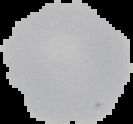 Image is 133×124 pixels. From a thin blood film. Segmented cell region on a black background. Malaria status: uninfected.